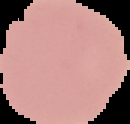
image_size: 130×124 pixels
image_type: cell region segmented out of the field of view; surrounding area masked to black
result: no Plasmodium parasites detected
preparation: thin blood film